Report the malaria status of this cell.
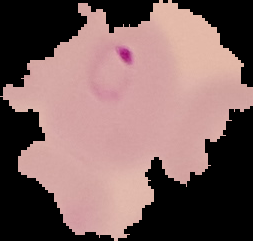

Parasitized.

Image is 253×241 pixels. The area outside the segmented cell region is set to black. From a thin blood film.